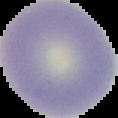
Summary:
  - Image size: 118×118 pixels
  - Image type: segmented cell region on a black background
  - Preparation: thin blood smear
  - Malaria status: uninfected